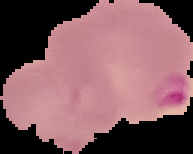

{
  "image_type": "segmented cell region with the area outside set to black",
  "result": "malaria parasites identified",
  "preparation": "thin blood film",
  "image_size": "193×154 pixels"
}